Identify the cell.
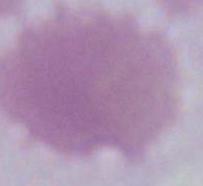
An erythrocyte.

Summary:
  - Modality: micrograph
  - Magnification: 1000x